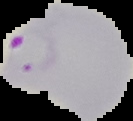

{
  "image_type": "segmented cell region on a black background",
  "preparation": "thin blood smear",
  "result": "Plasmodium parasites detected",
  "image_size": "133×121 pixels"
}